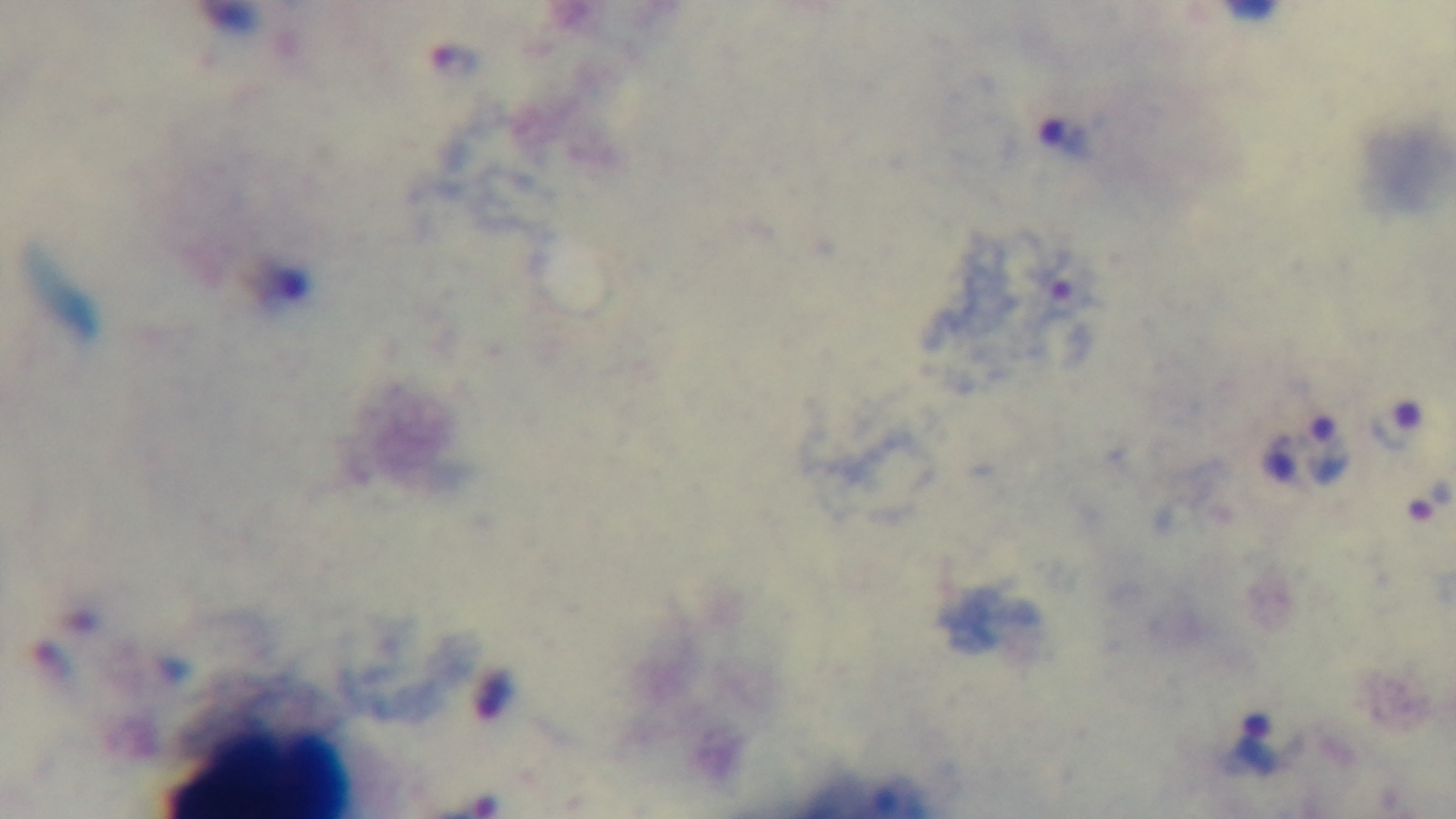
Summary:
  - Stain: Giemsa
  - Preparation: thick smear
  - Objective: 100x oil immersion
  - Capture: mounted 4K digital camera
  - Modality: light microscopy
  - Field of view: one from the slide
  - Malaria status: infected